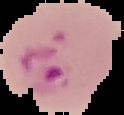
image_type: segmented cell region with the area outside set to black
image_size: 124×115 pixels
preparation: thin blood smear
malaria_status: parasitized